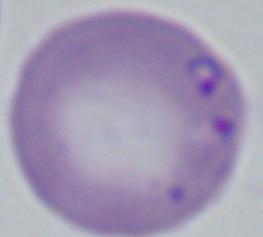

modality = photomicrograph
identification = Babesia
magnification = 1000x